Assess the morphology of the erythrocytes.
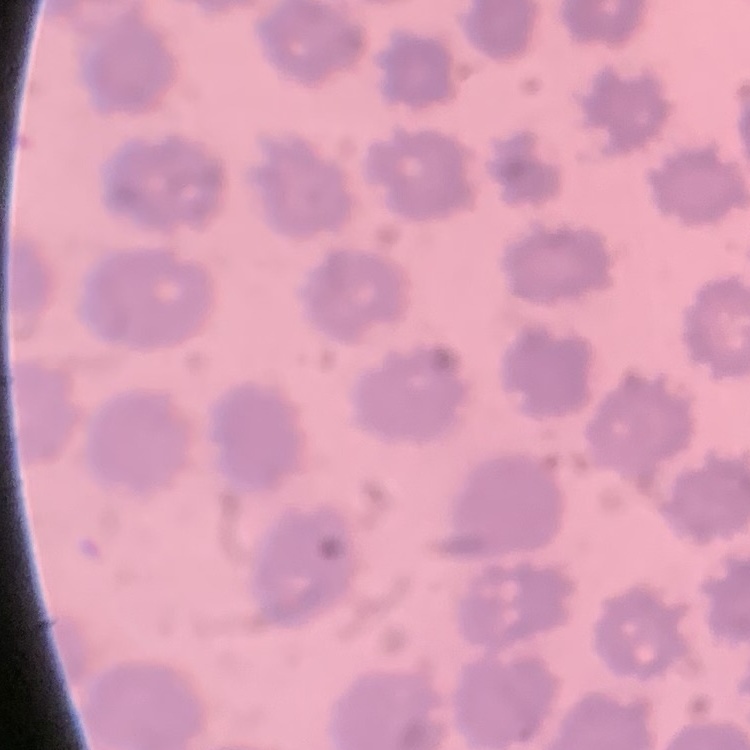
No rouleaux formation.

Summary:
  - Preparation: thin blood smear
  - Stain: Field's or Giemsa
  - Image type: square crop of a larger photomicrograph